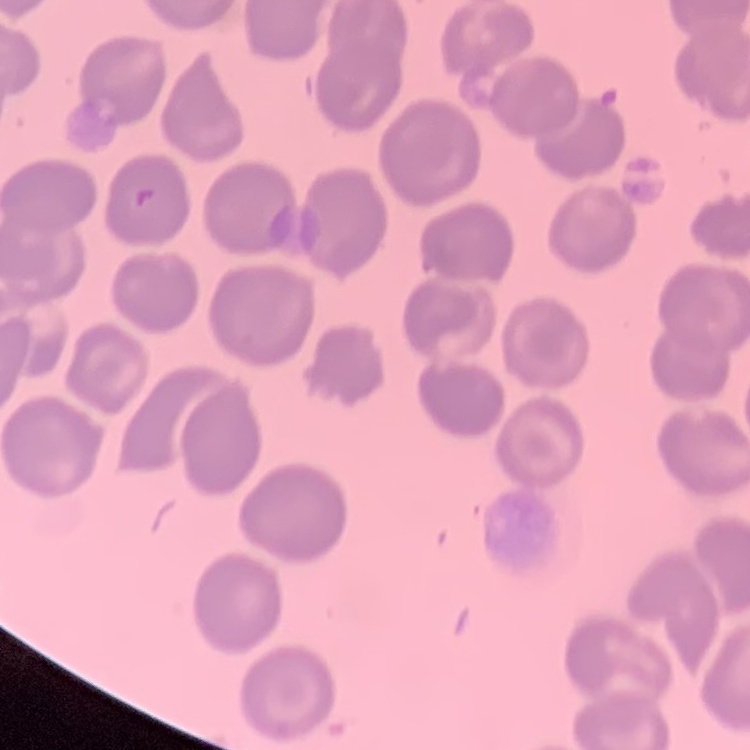
The erythrocytes show no rouleaux formation. Square crop of a larger photomicrograph. Thin blood smear. Field's or Giemsa stain.